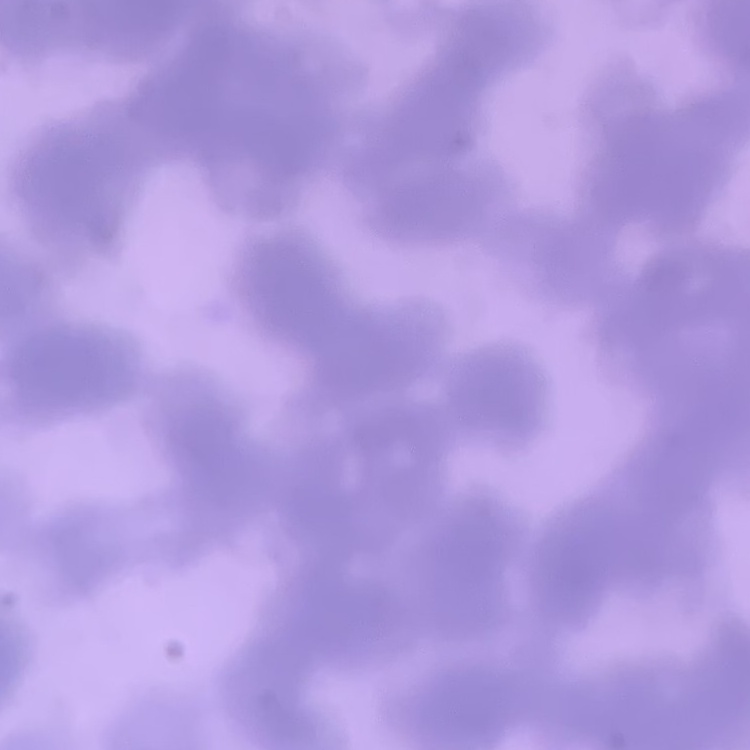

erythrocyte_morphology: rouleaux formation
preparation: thin peripheral smear
image_type: one tile cut from a larger photomicrograph
stain: Field's or Giemsa